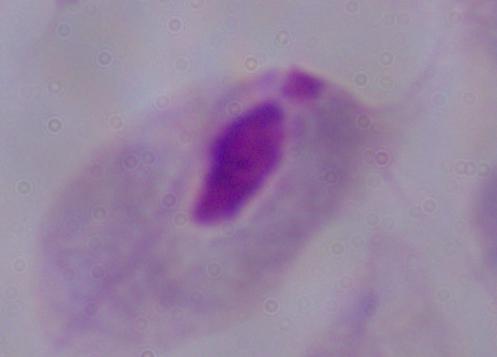

A trichomonad is shown. 1000x magnification. Micrograph.